Locate and identify every blood parasite.
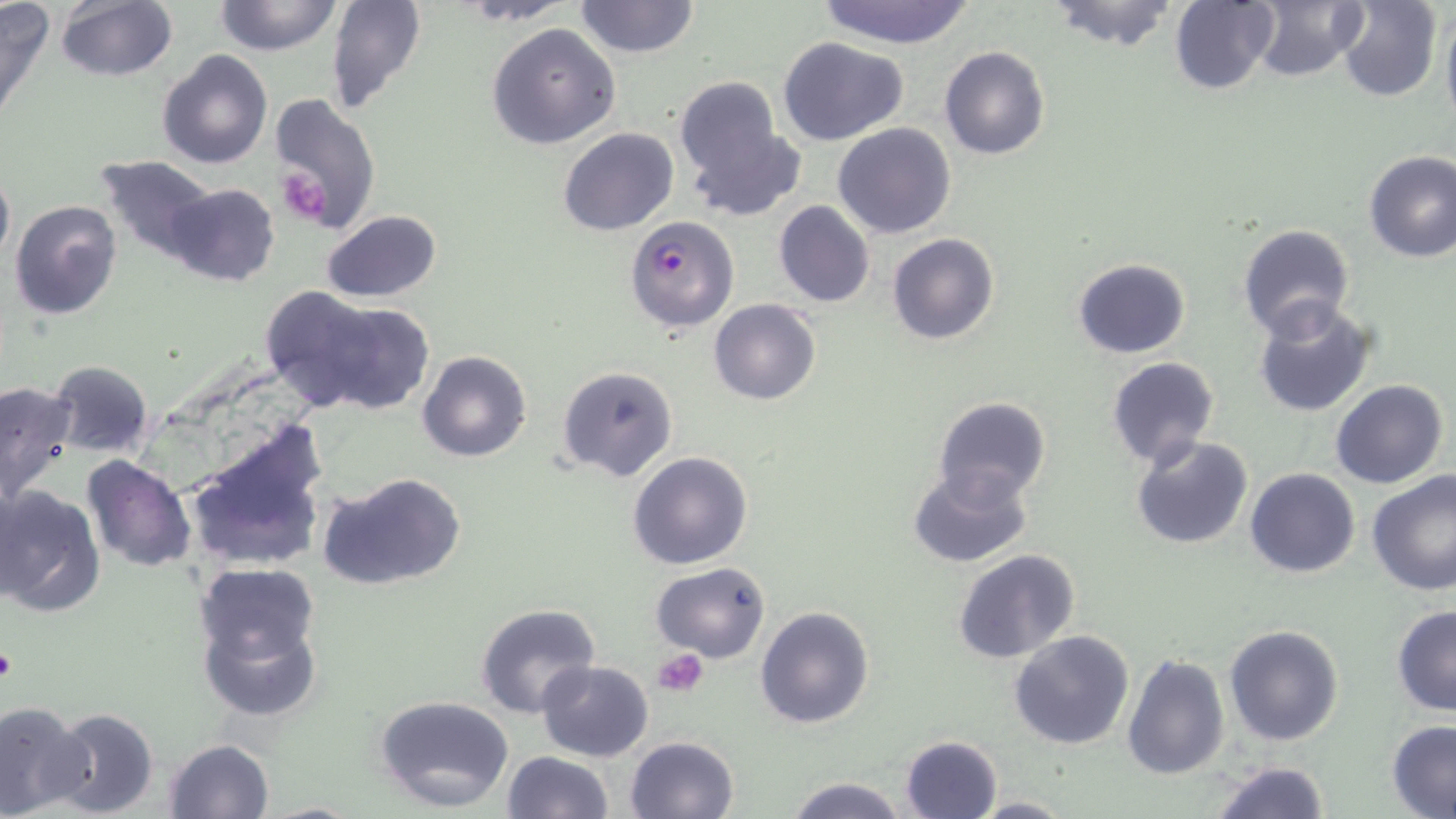

Approximate bounding boxes as named x1/y1/x2/y2 corners in pixels.
Plasmodium falciparum-infected red blood cells: (x1=624, y1=214, x2=739, y2=331).
No Plasmodium ovale, Plasmodium malariae, Plasmodium vivax, Babesia divergens, or Trypanosoma brucei observed.

slide-level diagnosis = Plasmodium falciparum
image size = 1456×819 pixels
preparation = thin blood smear
stain = May-Grünwald-Giemsa
field of view = single
platelet locations = approximate bounding boxes as named x1/y1/x2/y2 corners in pixels: (x1=276, y1=168, x2=331, y2=225), (x1=0, y1=642, x2=15, y2=686), (x1=655, y1=648, x2=707, y2=697)
modality = optical microscopy
magnification = 1000x
uninfected red blood cell locations = approximate bounding boxes as named x1/y1/x2/y2 corners in pixels: (x1=0, y1=0, x2=55, y2=127), (x1=214, y1=0, x2=343, y2=56), (x1=326, y1=0, x2=428, y2=115), (x1=574, y1=0, x2=700, y2=58), (x1=815, y1=0, x2=979, y2=48), (x1=1044, y1=0, x2=1182, y2=51), (x1=1339, y1=0, x2=1442, y2=102), (x1=1440, y1=0, x2=1456, y2=131), (x1=55, y1=1, x2=178, y2=82), (x1=462, y1=1, x2=570, y2=24), (x1=1168, y1=1, x2=1278, y2=93), (x1=1247, y1=1, x2=1368, y2=82), (x1=486, y1=24, x2=621, y2=150), (x1=778, y1=37, x2=910, y2=146), (x1=939, y1=46, x2=1051, y2=161), (x1=156, y1=48, x2=272, y2=169), (x1=675, y1=78, x2=799, y2=219), (x1=264, y1=92, x2=381, y2=233), (x1=833, y1=122, x2=958, y2=239), (x1=558, y1=128, x2=677, y2=236), (x1=1362, y1=149, x2=1456, y2=263), (x1=95, y1=154, x2=218, y2=262), (x1=0, y1=164, x2=14, y2=267), (x1=162, y1=181, x2=281, y2=287), (x1=9, y1=200, x2=122, y2=319), (x1=773, y1=200, x2=876, y2=308), (x1=319, y1=210, x2=443, y2=303), (x1=1237, y1=225, x2=1355, y2=340), (x1=888, y1=233, x2=998, y2=345), (x1=1072, y1=258, x2=1191, y2=359), (x1=280, y1=291, x2=432, y2=413), (x1=1252, y1=297, x2=1378, y2=417), (x1=710, y1=299, x2=820, y2=404), (x1=416, y1=349, x2=533, y2=463), (x1=1106, y1=358, x2=1219, y2=469), (x1=47, y1=360, x2=154, y2=458), (x1=557, y1=364, x2=680, y2=483), (x1=0, y1=378, x2=77, y2=504), (x1=1332, y1=380, x2=1447, y2=489), (x1=933, y1=396, x2=1051, y2=506), (x1=183, y1=420, x2=329, y2=574), (x1=1131, y1=434, x2=1253, y2=550), (x1=81, y1=453, x2=196, y2=573), (x1=627, y1=453, x2=752, y2=570), (x1=907, y1=465, x2=1034, y2=568), (x1=1246, y1=469, x2=1361, y2=579), (x1=1367, y1=469, x2=1456, y2=595), (x1=321, y1=470, x2=467, y2=591), (x1=0, y1=484, x2=105, y2=616), (x1=952, y1=548, x2=1082, y2=665), (x1=194, y1=561, x2=321, y2=672), (x1=651, y1=562, x2=771, y2=662), (x1=195, y1=600, x2=325, y2=725), (x1=475, y1=603, x2=600, y2=718), (x1=754, y1=605, x2=876, y2=730), (x1=1392, y1=606, x2=1456, y2=717), (x1=1224, y1=625, x2=1344, y2=746), (x1=1009, y1=630, x2=1134, y2=750), (x1=1122, y1=652, x2=1228, y2=777), (x1=536, y1=659, x2=652, y2=760), (x1=374, y1=693, x2=516, y2=813), (x1=0, y1=700, x2=92, y2=818), (x1=46, y1=707, x2=161, y2=818), (x1=1386, y1=720, x2=1456, y2=818), (x1=900, y1=734, x2=1002, y2=819), (x1=625, y1=735, x2=740, y2=819), (x1=164, y1=738, x2=274, y2=819), (x1=501, y1=750, x2=614, y2=819), (x1=1209, y1=760, x2=1331, y2=817), (x1=785, y1=775, x2=909, y2=818), (x1=973, y1=793, x2=1073, y2=816)